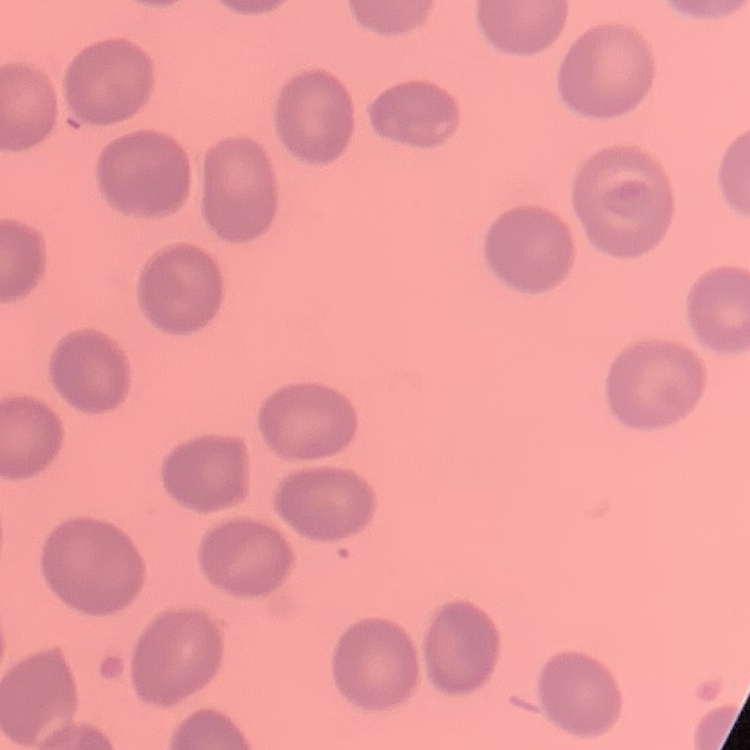
Summary:
  - Red blood cell morphology: no rouleaux formation
  - Stain: Field's or Giemsa
  - Image type: square crop of a larger photomicrograph
  - Preparation: thin blood film